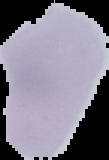
{
  "preparation": "thin blood film",
  "result": "negative for Plasmodium parasites",
  "image_type": "segmented cell region on a black background",
  "image_size": "109×160 pixels"
}